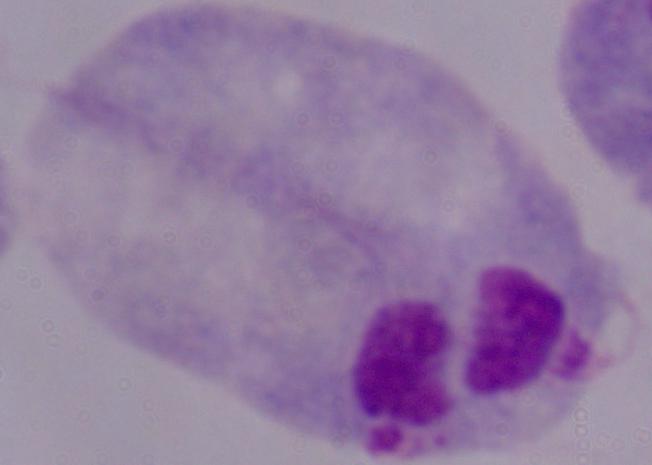 Photomicrograph. A trichomonad is seen. 1000x magnification.